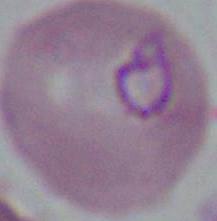
modality = photomicrograph
identification = Plasmodium
magnification = 400x or 1000x